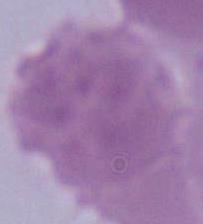
Micrograph. Captured at 1000x magnification. An erythrocyte is shown.